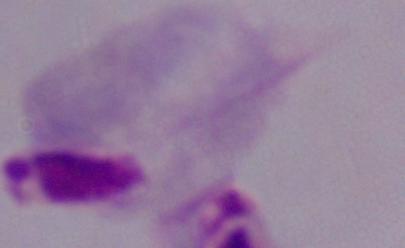

Summary:
  - Magnification: 1000x
  - Identification: trichomonad
  - Modality: photomicrograph